Evaluate for Plasmodium parasites.
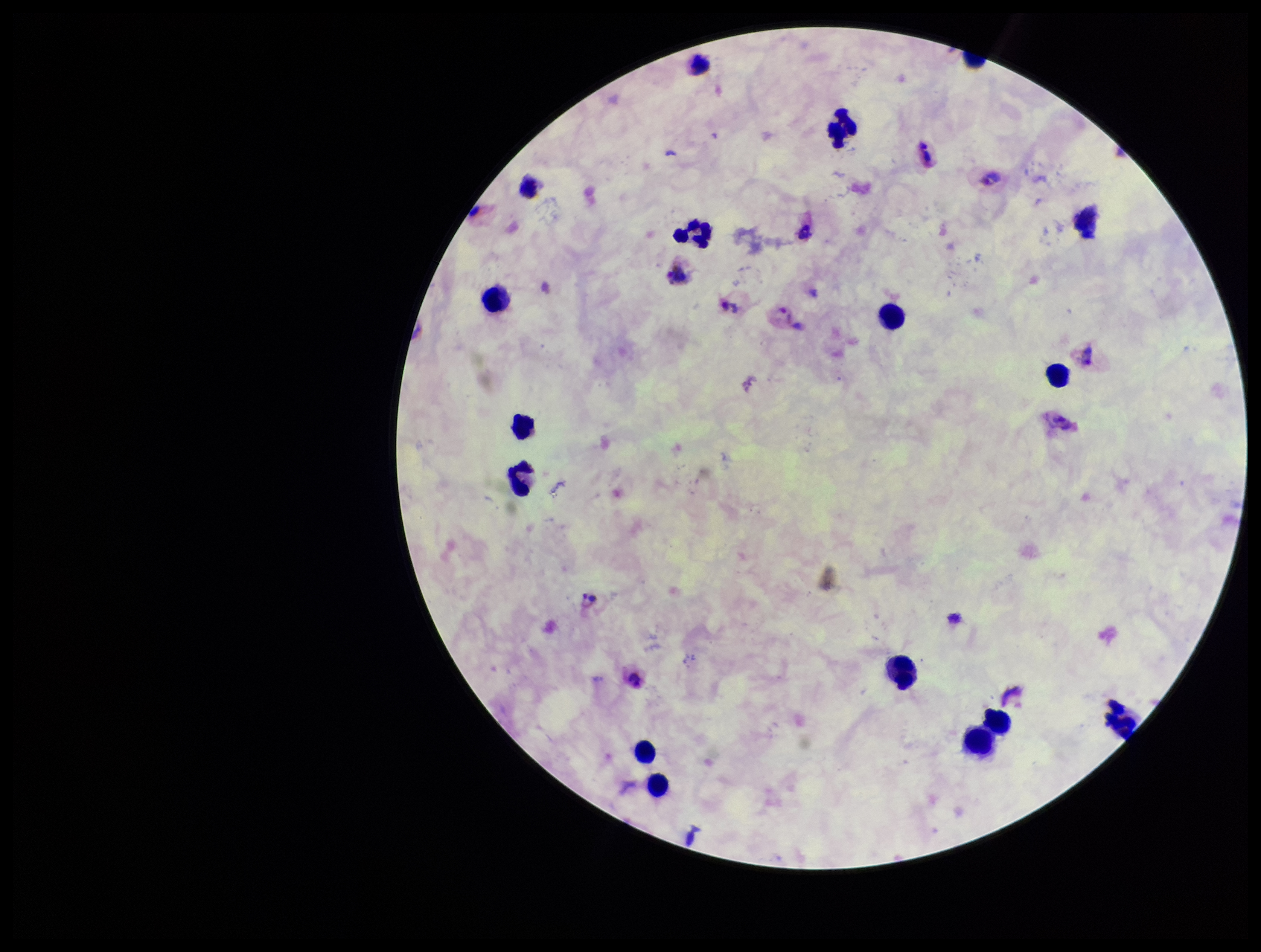

Seen.

Species reported for this patient: Plasmodium vivax. Parasite count: 5. Leukocyte count: 16. Patient malaria status: positive. Smartphone photograph taken through the eyepiece of a microscope. Preparation: thick. One field from this slide. Giemsa stain. Image is 1261×952 pixels.